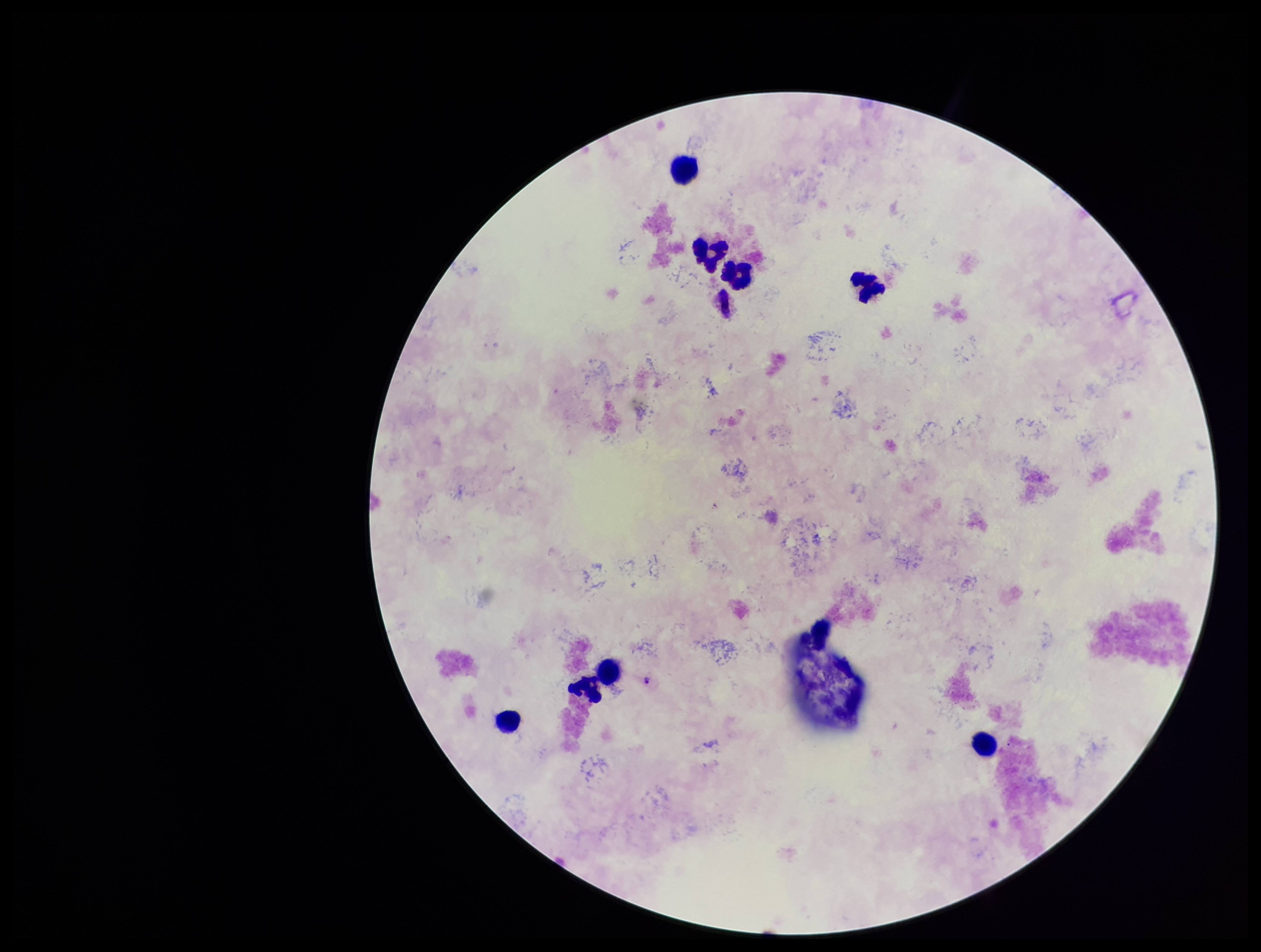

image_size: 1261×952 pixels
preparation: thick smear
patient_malaria_status: infected
parasite_count: 0
leukocyte_count: 8
stain: Giemsa
species_reported_for_this_patient: Plasmodium falciparum
field_of_view: single
plasmodium_parasites: none seen
capture: smartphone photograph through the microscope eyepiece